State the preparation type.
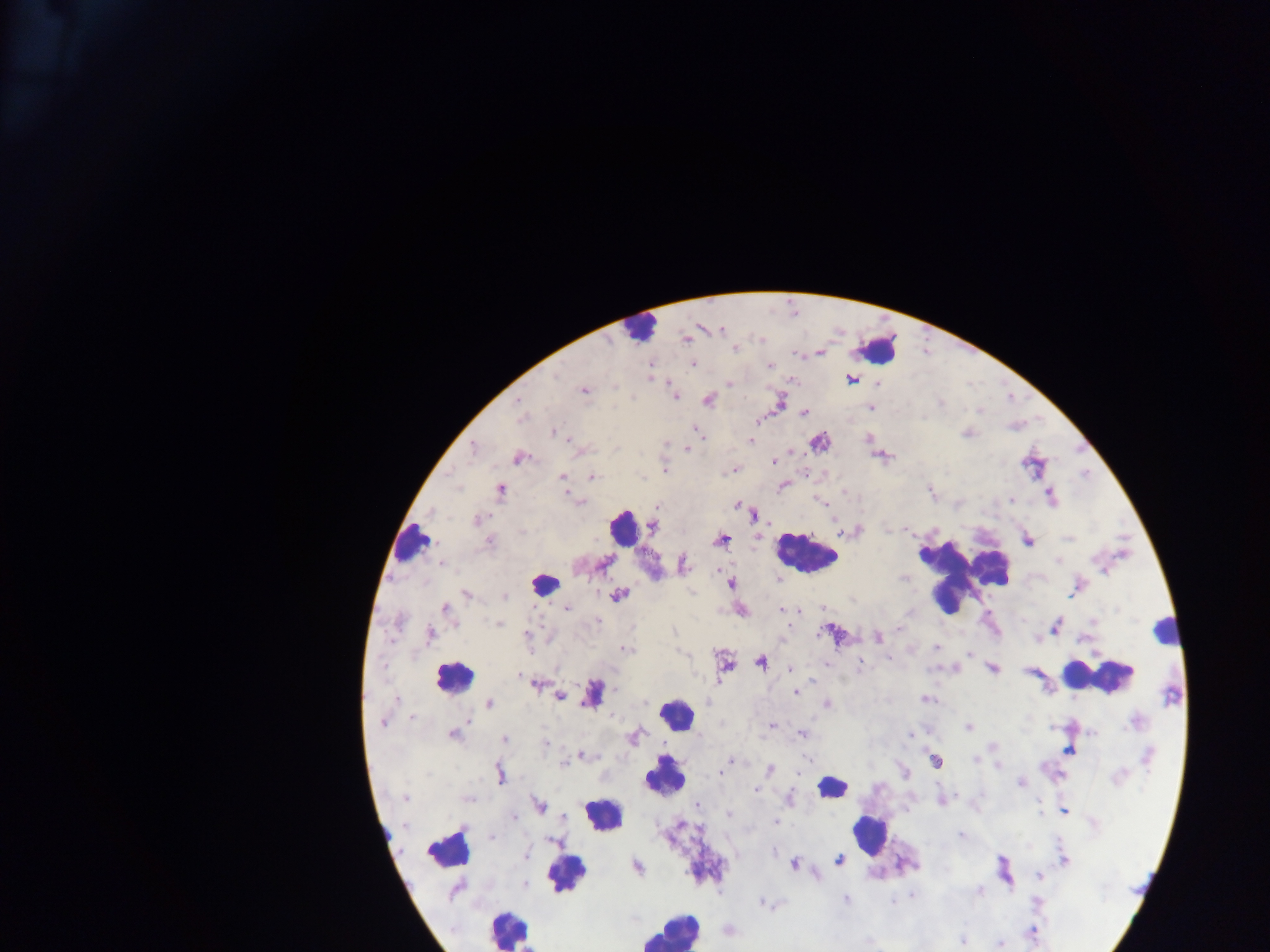

Thick blood smear.

field_of_view: single
country: Ghana
image_size: 1270×952 pixels
plasmodium_parasite_locations: 'approximate centers as {x, y} in pixels: {721, 329}, {735, 349}, {693, 365}, {770, 365}, {556, 376}, {851, 380}, {730, 383}, {584, 390}, {675, 397}, {519, 400}, {708, 400}, {780, 402}, {871, 407}, {804, 413}, {521, 419}, {758, 420}, {553, 432}, {699, 433}, {751, 441}, {819, 443}, {474, 448}, {615, 448}, {687, 449}, {518, 459}, {774, 461}, {665, 469}, {733, 471}, {592, 477}, {562, 478}, {783, 486}, {457, 488}, {501, 490}, {1050, 497}, {1011, 500}, {581, 502}, {823, 504}, {737, 505}, {657, 508}, {753, 515}, {476, 522}, {653, 527}, {721, 540}, {1028, 540}, {490, 542}, {683, 564}, {442, 565}, {777, 579}, {730, 583}, {619, 594}, {466, 595}, {504, 596}, {567, 608}, {445, 610}, {783, 610}, {741, 611}, {598, 621}, {498, 623}, {1055, 626}, {900, 628}, {674, 630}, {831, 633}, {431, 635}, {528, 635}, {877, 637}, {936, 647}, {625, 650}, {970, 653}, {761, 661}, {860, 664}, {725, 666}, {791, 669}, {993, 669}, {519, 676}, {536, 684}, {796, 692}, {591, 694}, {559, 697}, {926, 699}, {489, 703}, {826, 704}, {412, 719}, {1135, 722}, {382, 723}, {772, 725}, {968, 727}, {1092, 732}, {453, 734}, {803, 734}, {910, 735}, {633, 737}, {505, 738}, {545, 744}, {993, 746}, {1068, 751}, {582, 755}, {1148, 756}, {732, 760}, {975, 760}, {936, 762}, {564, 764}, {998, 765}, {769, 769}, {720, 773}, {500, 774}, {1118, 777}, {1020, 783}, {756, 790}, {405, 798}, {789, 798}, {468, 799}, {942, 800}, {698, 804}, {539, 805}, {1064, 811}, {729, 815}, {513, 817}, {775, 822}, {1093, 823}, {960, 835}, {492, 838}, {553, 840}, {526, 855}, {839, 860}, {1064, 860}, {794, 864}, {637, 867}, {1038, 876}, {524, 884}, {456, 890}, {979, 891}, {911, 895}, {845, 900}, {893, 902}, {1036, 903}, {761, 904}, {1032, 932}, {962, 940}, {1000, 944}'
capture: mobile-phone photograph through a microscope
leukocyte_locations: 'approximate centers as {x, y} in pixels: {638, 328}, {880, 348}, {622, 528}, {412, 540}, {805, 553}, {962, 575}, {544, 583}, {1170, 630}, {1097, 677}, {453, 678}, {675, 713}, {665, 776}, {832, 788}, {602, 816}, {869, 832}, {444, 850}, {571, 875}, {508, 929}, {669, 931}'